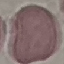

malaria_status: uninfected
stain: Giemsa
preparation: thin blood film
image_type: automatically extracted cell patch, resized to 64 × 64 pixels
capture: smartphone camera at the microscope eyepiece